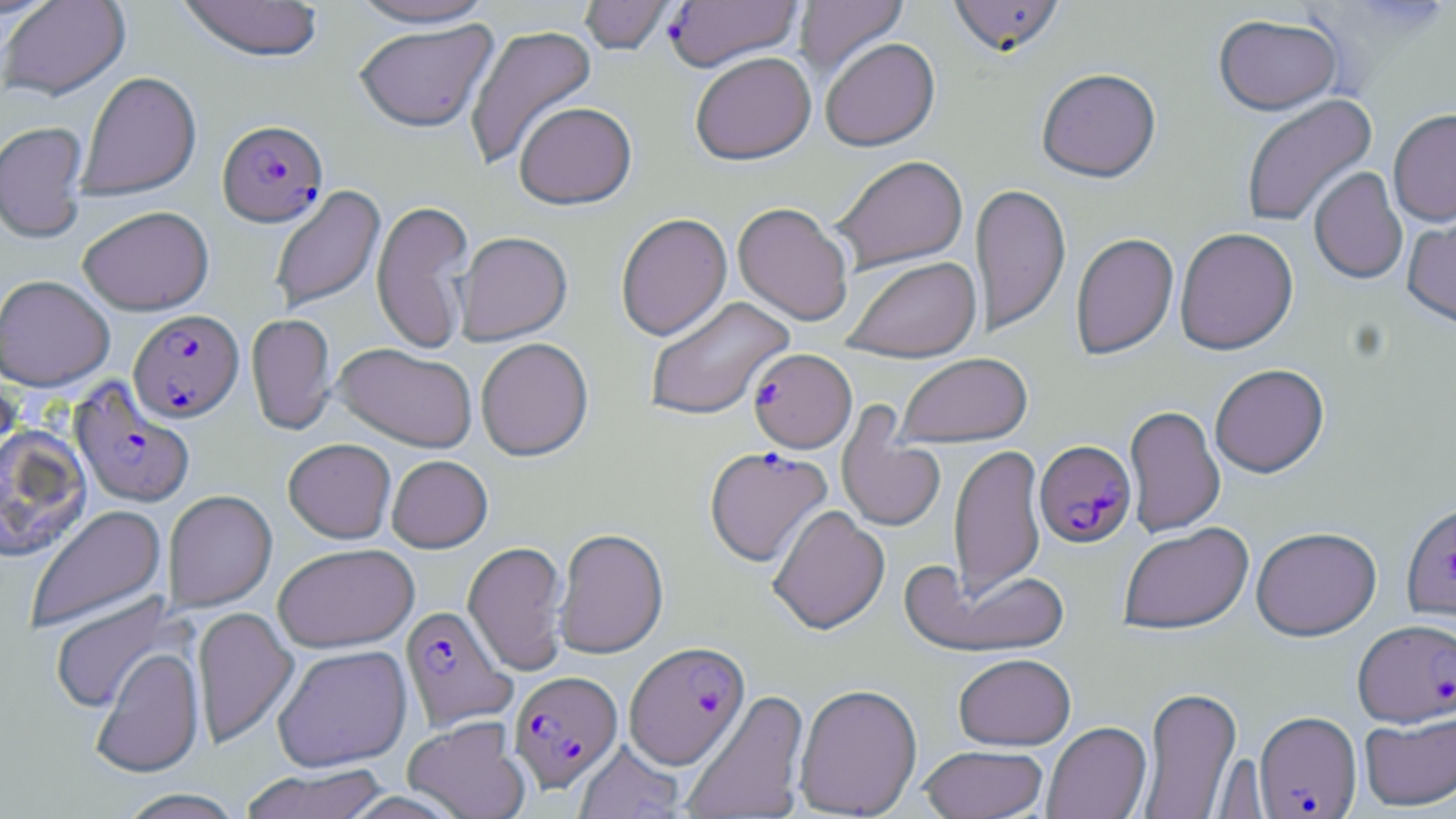

slide-level diagnosis = Plasmodium falciparum
field of view = single
image size = 1456×819 pixels
Plasmodium falciparum-infected red blood cell locations = approximate bounding boxes as (x1, y1, x2, y2) in pixels: (664, 1, 803, 73), (217, 121, 329, 229), (128, 309, 245, 424), (749, 349, 856, 453), (69, 379, 195, 509), (1034, 441, 1137, 550), (705, 446, 833, 569), (1402, 504, 1456, 625), (400, 605, 516, 731), (1353, 620, 1456, 729), (624, 642, 750, 771), (509, 671, 623, 793), (1254, 712, 1362, 818)
magnification = 1000x
preparation = thin blood film
uninfected red blood cell locations = approximate bounding boxes as (x1, y1, x2, y2) in pixels: (0, 0, 131, 102), (178, 0, 324, 64), (345, 0, 499, 31), (579, 0, 678, 57), (794, 0, 909, 82), (948, 0, 1066, 60), (1214, 16, 1343, 118), (354, 21, 498, 134), (464, 24, 599, 171), (821, 39, 940, 154), (690, 53, 816, 168), (1036, 70, 1162, 185), (78, 72, 202, 203), (1241, 94, 1378, 228), (515, 103, 638, 212), (1388, 112, 1456, 229), (0, 122, 89, 244), (832, 156, 968, 275), (1309, 168, 1408, 285), (971, 183, 1071, 337), (269, 184, 386, 315), (372, 200, 475, 354), (732, 203, 852, 327), (77, 206, 214, 316), (1402, 210, 1456, 333), (616, 214, 732, 342), (1175, 228, 1298, 356), (455, 232, 573, 346), (1071, 233, 1179, 360), (843, 257, 982, 364), (0, 275, 115, 392), (645, 296, 794, 422), (247, 314, 337, 436), (476, 338, 594, 462), (333, 343, 477, 453), (896, 354, 1032, 448), (1210, 364, 1329, 480), (0, 373, 23, 478), (836, 405, 946, 535), (1124, 405, 1225, 538), (0, 425, 92, 563), (283, 439, 396, 544), (949, 443, 1046, 602), (386, 455, 493, 553), (163, 490, 277, 612), (24, 504, 168, 634), (767, 506, 890, 637), (1118, 524, 1254, 636), (553, 528, 669, 660), (1251, 528, 1382, 643), (463, 540, 570, 677), (273, 543, 419, 653), (904, 563, 1071, 659), (48, 591, 185, 716), (191, 606, 299, 750), (271, 644, 413, 772), (90, 647, 204, 778), (953, 655, 1076, 752), (794, 683, 923, 819), (1139, 687, 1243, 817), (681, 690, 809, 818), (1359, 713, 1456, 812), (402, 716, 531, 819), (1042, 723, 1152, 819), (573, 740, 686, 819), (919, 745, 1048, 819), (238, 763, 391, 819), (115, 788, 247, 819)
modality = optical microscopy
stain = May-Grünwald-Giemsa